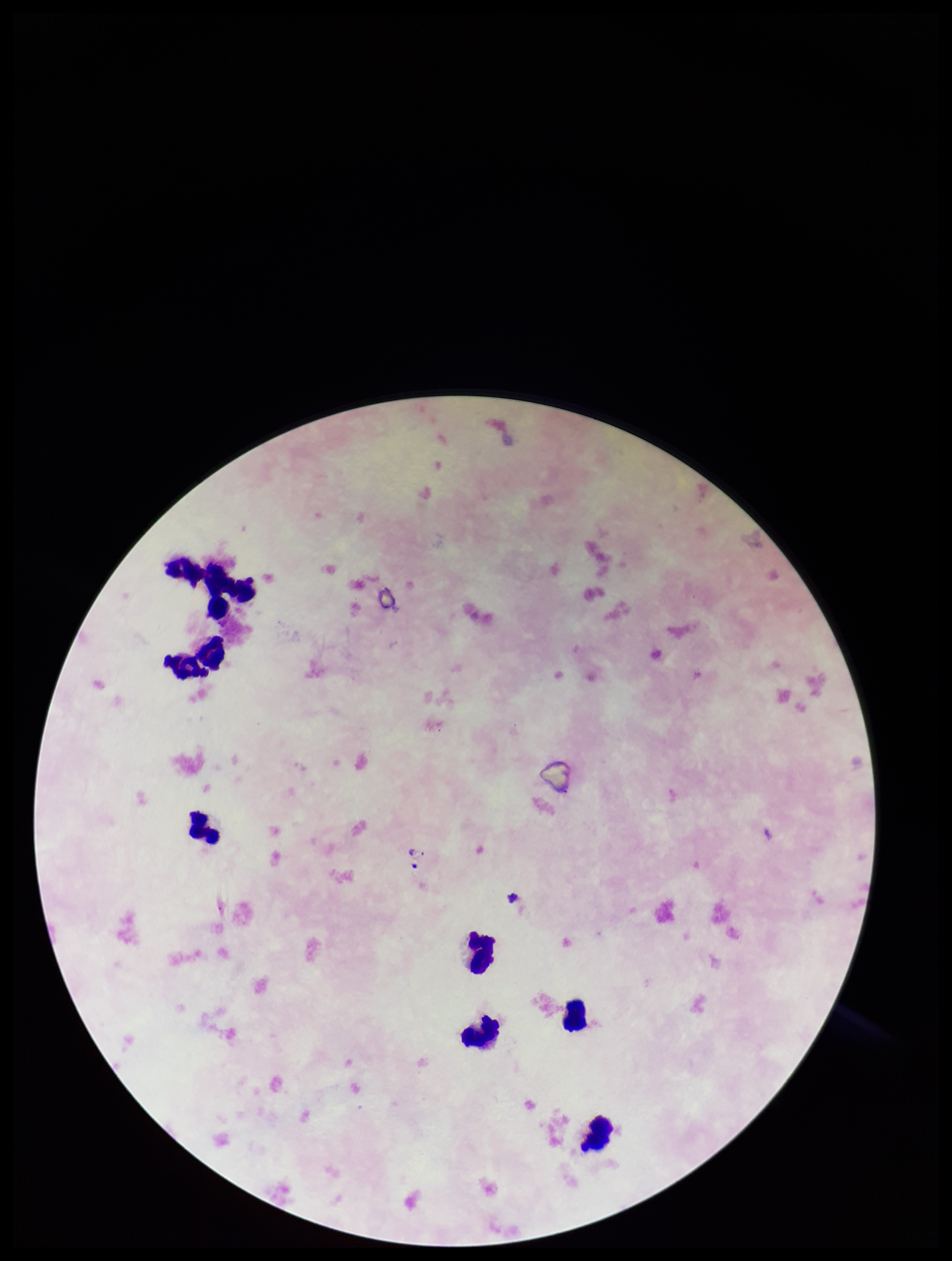

Summary:
  - Field of view: single
  - Capture: smartphone photograph through the microscope eyepiece
  - Leukocyte count: 9
  - Plasmodium parasites: none detected
  - Image size: 952×1261 pixels
  - Stain: Giemsa
  - Patient malaria status: negative
  - Preparation: thick smear
  - Parasite count: 0